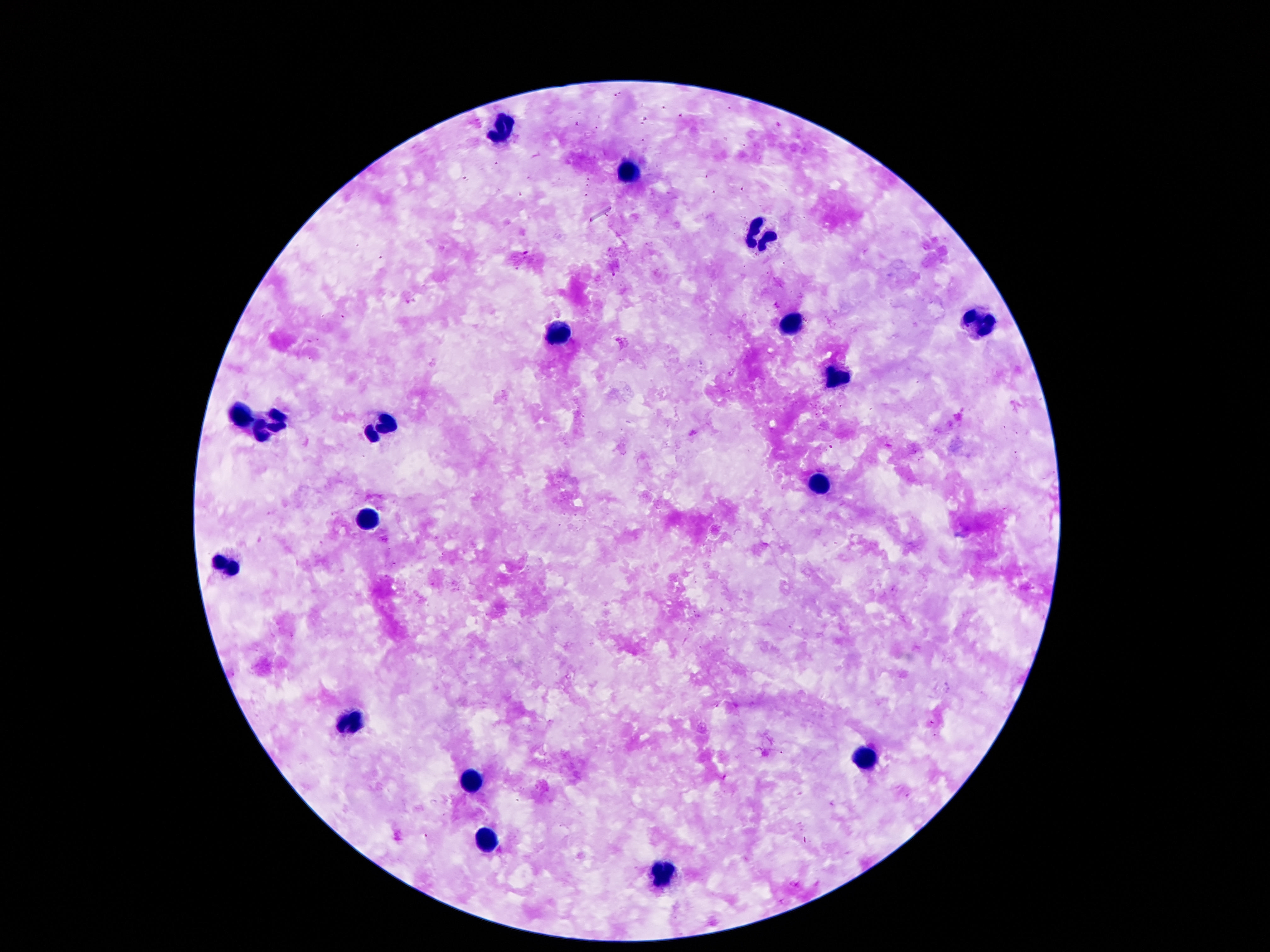
preparation = thick blood film
image size = 1270×952 pixels
stain = Giemsa
patient malaria status = uninfected
field of view = one from this slide
magnification = 100x
leukocyte locations = approximate centers as (x, y) in pixels: (501, 129), (629, 172), (756, 236), (788, 325), (978, 325), (560, 332), (835, 381), (238, 418), (270, 428), (379, 429), (815, 486), (368, 518), (225, 566), (352, 725), (862, 759), (470, 779), (484, 843), (661, 875)
capture = smartphone camera through the microscope eyepiece